Comment on the morphology of the red blood cells.
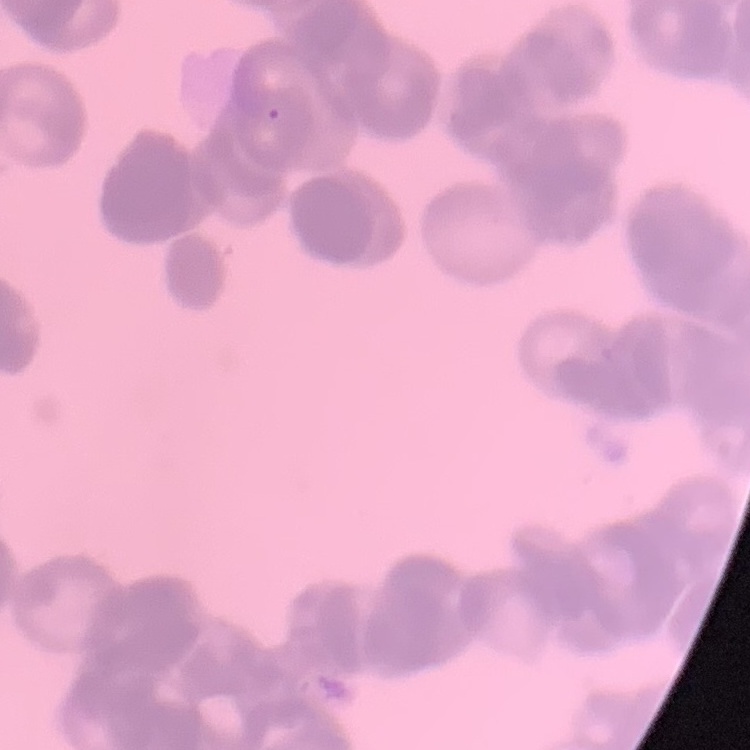

Rouleaux formation.

{
  "preparation": "thin blood film",
  "stain": "Field's or Giemsa",
  "image_type": "square crop of a larger photomicrograph"
}